Assess the morphology of the red blood cells.
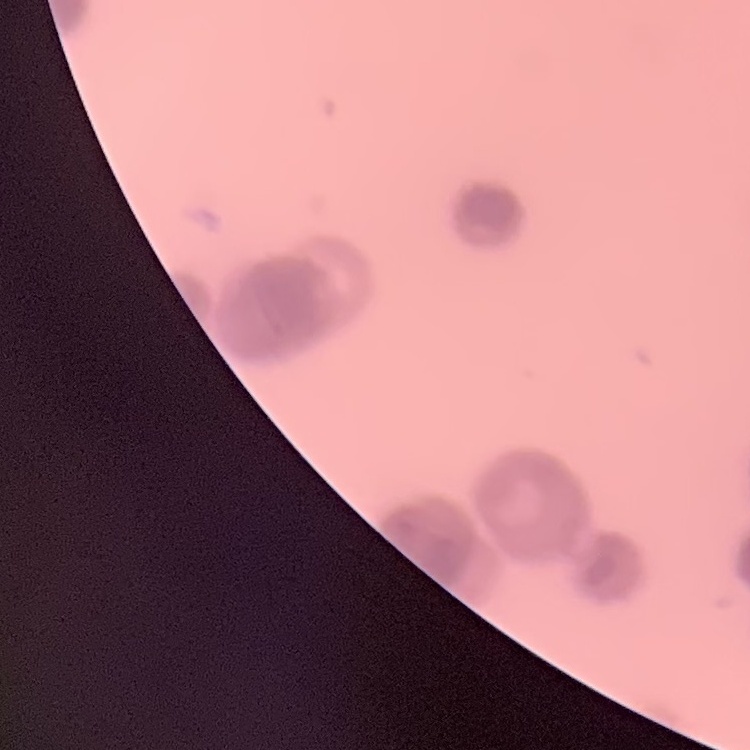

They show rouleaux formation.

Thin peripheral smear. Field's or Giemsa stain. Square crop of a larger photomicrograph.